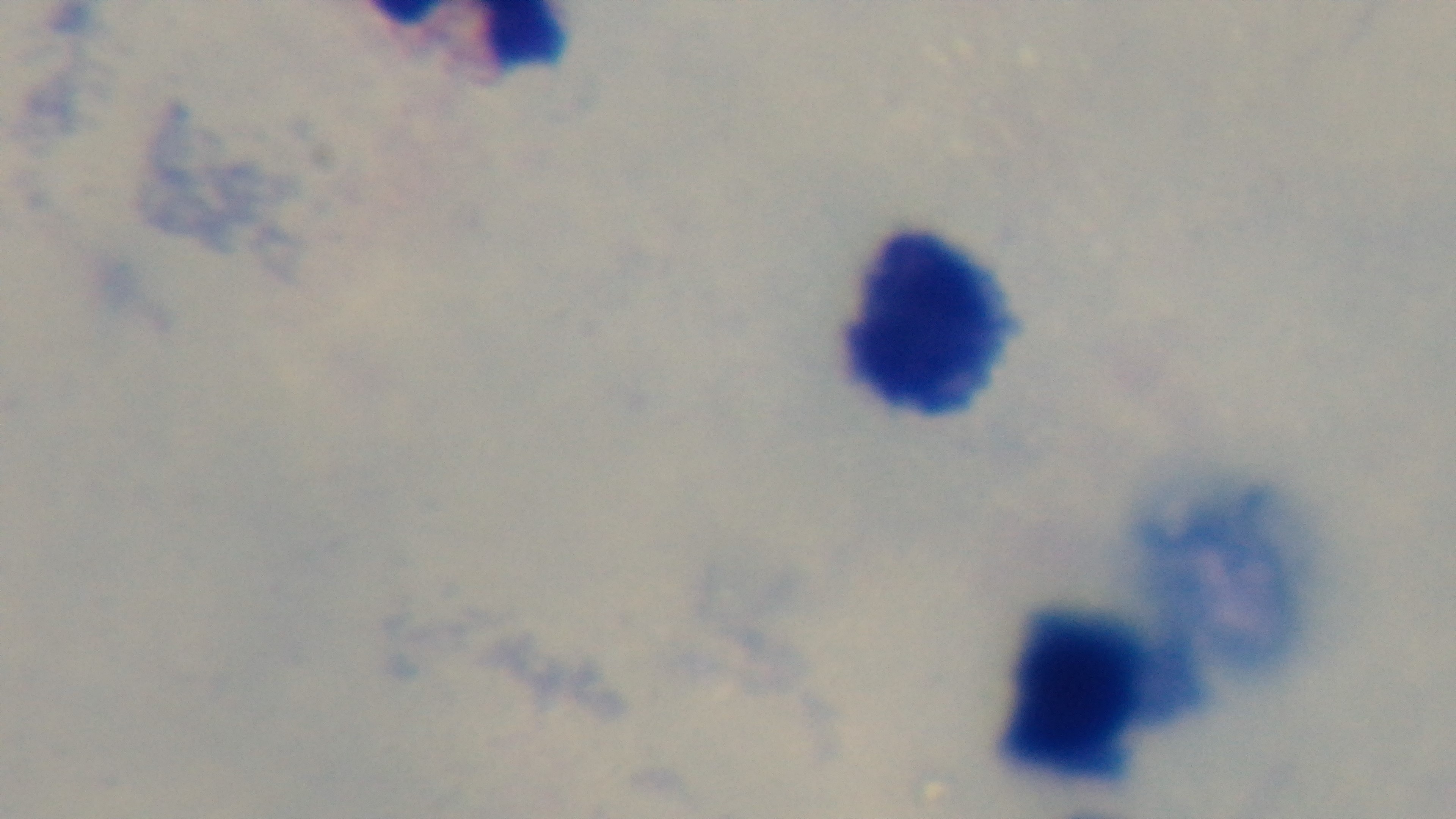

100x oil-immersion objective. Mounted 4K digital camera. Photomicrograph. Malaria status: uninfected. One field from the slide. Preparation: thick smear. Giemsa stain.